Outline each Plasmodium falciparum-infected red blood cell.
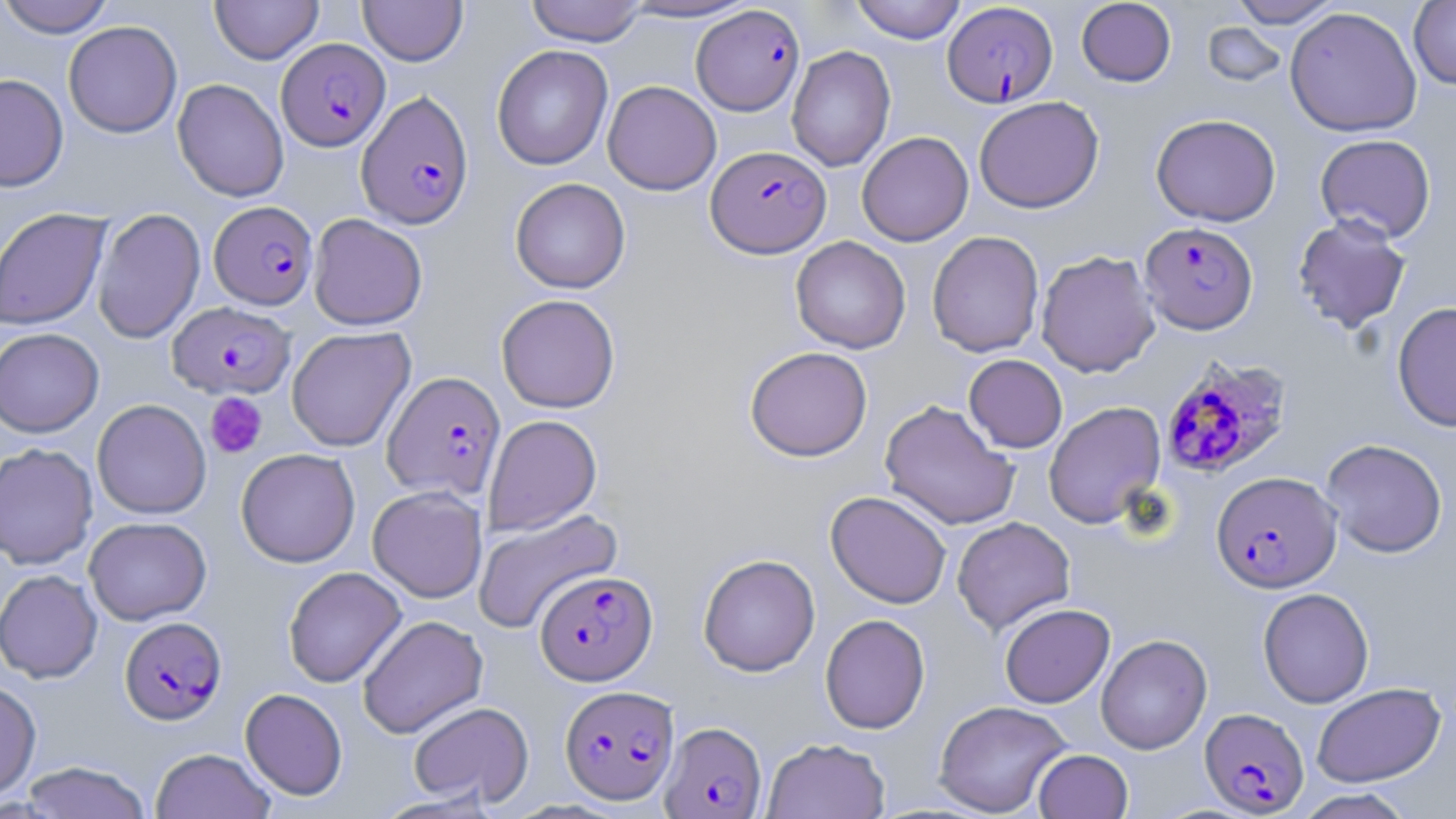
Approximate bounding boxes as (x1, y1, x2, y2) in pixels.
Plasmodium falciparum-infected red blood cells: (943, 3, 1058, 107), (691, 4, 805, 116), (276, 38, 390, 151), (356, 91, 473, 229), (706, 145, 831, 258), (209, 201, 318, 310), (1139, 221, 1259, 335), (167, 301, 295, 400), (1159, 355, 1292, 480), (382, 370, 506, 501), (1211, 470, 1341, 593), (535, 569, 657, 686), (120, 616, 226, 724), (560, 684, 679, 804), (1199, 707, 1309, 816), (660, 721, 767, 818).

{
  "slide_level_diagnosis": "Plasmodium falciparum",
  "modality": "light microscopy",
  "preparation": "thin blood smear",
  "uninfected_red_blood_cell_locations": "approximate bounding boxes as (x1, y1, x2, y2) in pixels: (0, 0, 115, 38), (358, 0, 467, 65), (525, 0, 648, 47), (616, 0, 762, 22), (850, 0, 966, 44), (1076, 0, 1176, 87), (1227, 0, 1344, 28), (210, 1, 324, 64), (1408, 1, 1456, 89), (1284, 6, 1423, 137), (63, 21, 182, 138), (1202, 22, 1287, 87), (491, 45, 613, 170), (786, 45, 896, 172), (0, 74, 69, 192), (172, 79, 289, 202), (602, 80, 721, 195), (974, 96, 1104, 214), (1151, 113, 1281, 226), (857, 131, 973, 246), (1315, 134, 1437, 243), (510, 177, 631, 293), (0, 207, 111, 331), (92, 208, 206, 343), (308, 214, 428, 330), (1292, 214, 1412, 334), (927, 230, 1044, 357), (790, 236, 911, 354), (1036, 249, 1161, 377), (496, 294, 620, 413), (1392, 301, 1456, 431), (0, 327, 104, 438), (286, 327, 416, 451), (744, 346, 873, 462), (963, 354, 1068, 453), (92, 399, 211, 519), (879, 399, 1020, 531), (1044, 401, 1166, 528), (483, 415, 602, 535), (1320, 438, 1448, 558), (0, 442, 98, 569), (236, 448, 360, 567), (367, 486, 487, 602), (825, 490, 951, 609), (472, 507, 623, 634), (951, 516, 1075, 635), (84, 517, 211, 625), (698, 553, 820, 677), (283, 566, 406, 688), (0, 569, 103, 683), (1258, 587, 1374, 708), (999, 603, 1115, 708), (820, 613, 930, 734), (357, 614, 488, 739), (1096, 633, 1212, 754), (0, 679, 41, 800), (1311, 682, 1446, 787), (240, 688, 348, 800), (933, 700, 1072, 817), (408, 701, 534, 808), (762, 737, 890, 819), (150, 747, 275, 819), (1033, 748, 1133, 819), (19, 761, 151, 819), (1292, 788, 1417, 818)",
  "field_of_view": "single",
  "image_size": "1456×819 pixels",
  "magnification": "1000x",
  "stain": "May-Grünwald-Giemsa",
  "platelet_locations": "approximate bounding boxes as (x1, y1, x2, y2) in pixels: (205, 392, 267, 459)"
}